Report the malaria status of this cell.
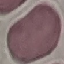
Uninfected.

Acquired by smartphone through the microscope eyepiece. Giemsa stain. Thin blood smear. Cell patch, automatically extracted from a larger field of view and resized to 64 × 64 pixels.